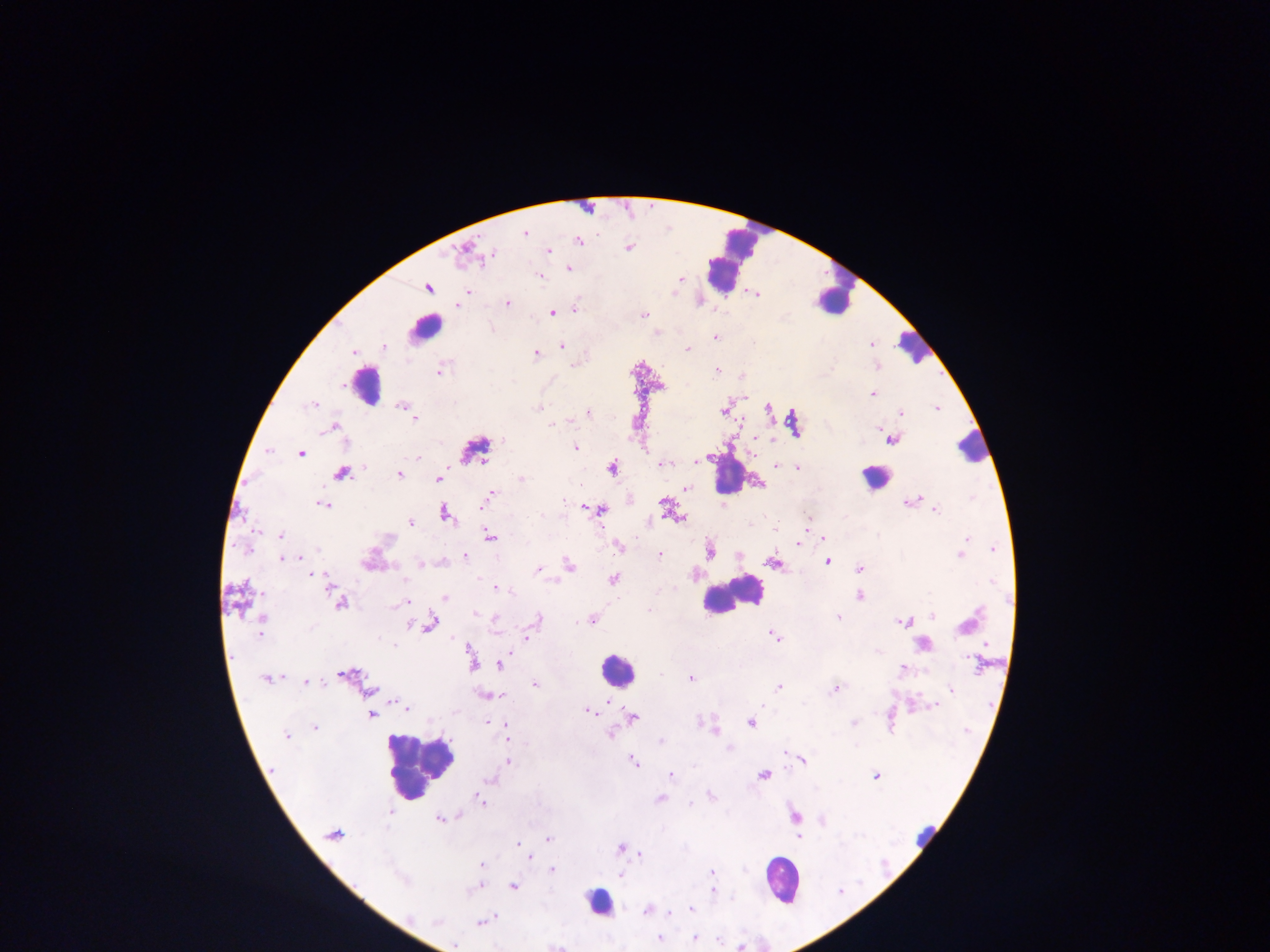

Approximate centers as (x, y) in pixels.
Summary:
  - Malaria parasite locations: (525, 232), (578, 241), (629, 248), (464, 250), (547, 251), (490, 255), (568, 268), (539, 275), (680, 279), (428, 287), (469, 290), (756, 294), (506, 303), (456, 304), (574, 309), (550, 312), (644, 314), (715, 337), (871, 344), (561, 345), (384, 346), (687, 349), (352, 351), (536, 353), (877, 367), (439, 370), (716, 370), (742, 376), (872, 393), (313, 404), (403, 406), (768, 407), (936, 407), (539, 408), (724, 410), (587, 411), (901, 413), (415, 418), (794, 422), (552, 424), (333, 426), (892, 438), (754, 439), (503, 440), (575, 448), (267, 450), (300, 453), (417, 458), (695, 461), (664, 464), (775, 465), (612, 467), (797, 467), (341, 473), (398, 473), (438, 479), (521, 480), (758, 483), (686, 487), (489, 496), (910, 501), (664, 503), (323, 504), (583, 507), (600, 510), (934, 510), (444, 512), (679, 517), (409, 522), (281, 535), (488, 535), (822, 537), (798, 545), (619, 546), (993, 549), (709, 550), (960, 553), (659, 554), (465, 555), (283, 558), (297, 558), (827, 560), (370, 561), (774, 562), (420, 565), (567, 565), (860, 568), (538, 569), (315, 575), (613, 579), (496, 588), (335, 592), (859, 595), (444, 597), (237, 599), (407, 600), (339, 603), (476, 613), (933, 615), (495, 618), (838, 618), (592, 619), (261, 620), (536, 620), (904, 622), (429, 623), (260, 632), (773, 635), (526, 638), (921, 644), (469, 650), (502, 660), (471, 662), (498, 664), (901, 670), (345, 675), (268, 678), (690, 678), (305, 682), (534, 684), (778, 686), (836, 688), (950, 688), (369, 691), (486, 695), (604, 701), (396, 702), (934, 704), (406, 707), (587, 711), (371, 714), (631, 717), (750, 722), (489, 723), (853, 723), (505, 724), (314, 727), (713, 730), (610, 733), (286, 736), (507, 738), (661, 741), (784, 750), (801, 759), (632, 760), (507, 762), (671, 774), (764, 775), (876, 775), (489, 779), (710, 796), (660, 799), (480, 801), (391, 812), (457, 815), (795, 815), (440, 819), (820, 819), (333, 834), (798, 835), (547, 839), (519, 843), (522, 848), (620, 848), (640, 853), (529, 857), (480, 864), (551, 870), (711, 872), (621, 875), (478, 884), (512, 886), (712, 891), (691, 909), (648, 910), (669, 915), (495, 916), (481, 922), (659, 938), (693, 938), (717, 939), (453, 945), (554, 945)
  - Leukocyte locations: (727, 258), (833, 292), (425, 328), (912, 346), (365, 384), (973, 446), (474, 449), (728, 474), (876, 478), (731, 594), (615, 670), (415, 763), (926, 836), (782, 879), (599, 901)
  - Field of view: single
  - Country: Ghana
  - Capture: mobile-phone photograph through a microscope
  - Preparation: thick blood film
  - Image size: 1270×952 pixels